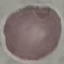

Summary:
  - Malaria status: uninfected
  - Preparation: thin blood film
  - Image type: automatically extracted cell patch, resized to 64 × 64 pixels
  - Stain: Giemsa
  - Capture: smartphone through the microscope eyepiece